Outline each Plasmodium ovale-infected red blood cell.
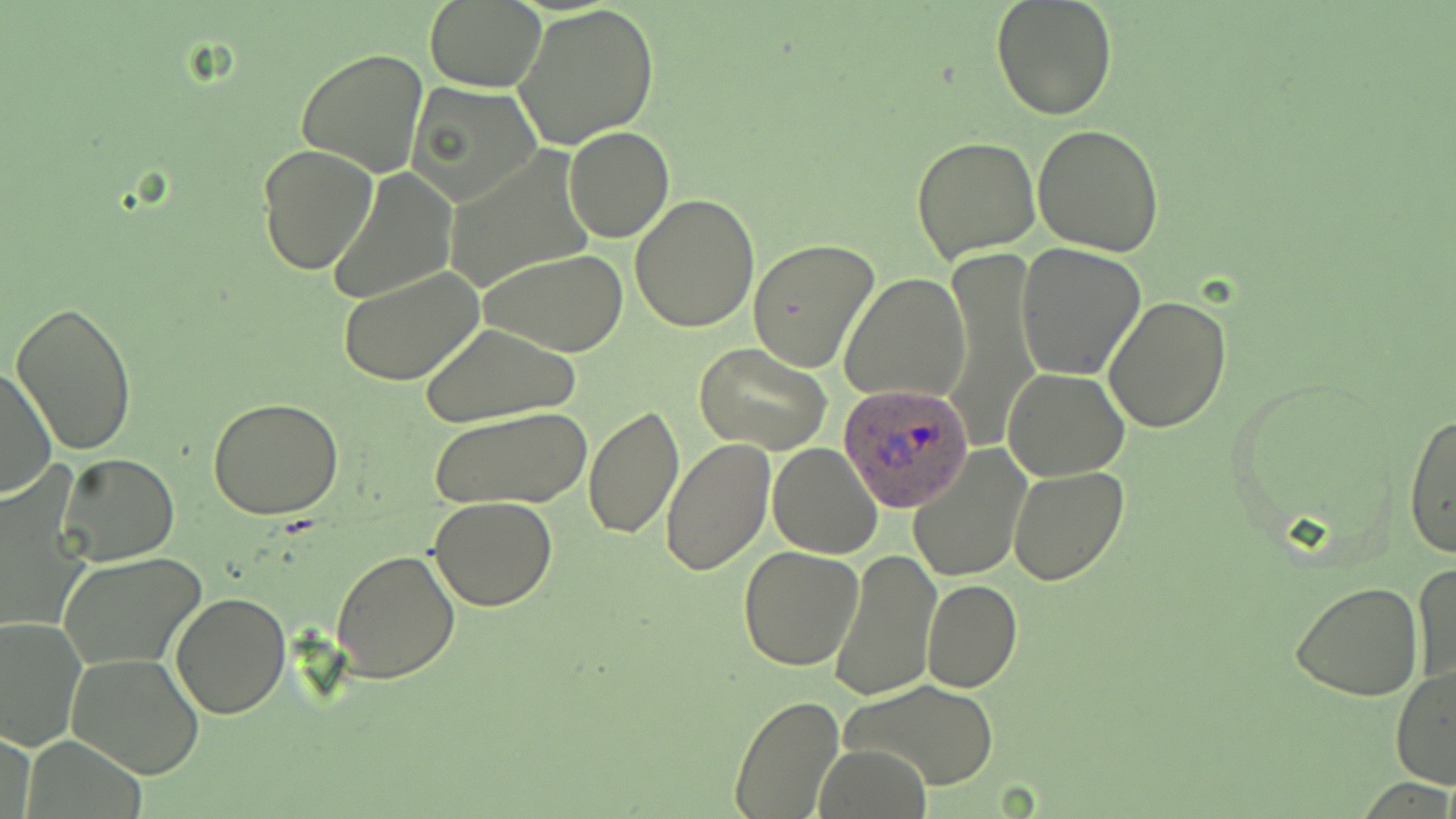
Approximate bounding boxes as (x1,y1)-(x2,y2) corner pairs in pixels.
Plasmodium ovale-infected red blood cells: (837,381)-(974,512).

Summary:
  - Uninfected red blood cell locations: (425,0)-(545,92), (989,0)-(1118,121), (513,2)-(662,148), (295,47)-(428,176), (406,81)-(543,208), (1032,121)-(1166,257), (563,127)-(674,243), (911,135)-(1042,264), (257,145)-(379,278), (444,150)-(598,294), (325,169)-(457,304), (629,193)-(760,332), (748,238)-(880,371), (1016,243)-(1147,380), (945,245)-(1039,448), (481,249)-(628,357), (335,265)-(487,386), (839,273)-(969,404), (1103,295)-(1233,433), (10,301)-(140,456), (421,323)-(580,427), (695,343)-(833,454), (0,364)-(56,500), (1003,366)-(1130,480), (209,397)-(345,519), (585,405)-(684,541), (428,406)-(592,509), (1402,410)-(1456,559), (659,437)-(775,575), (767,441)-(883,558), (907,446)-(1031,583), (57,453)-(178,565), (1008,465)-(1128,585), (1,474)-(92,635), (428,497)-(558,611), (738,545)-(865,670), (829,548)-(942,697), (330,549)-(461,684), (56,552)-(206,670), (1411,560)-(1455,691), (921,578)-(1023,693), (1290,579)-(1424,700), (170,592)-(291,720), (0,615)-(90,752), (67,652)-(205,779), (1391,664)-(1456,792), (843,681)-(1000,792), (728,695)-(845,818), (2,728)-(37,819), (815,745)-(931,819)
  - Slide-level diagnosis: Plasmodium ovale
  - Image size: 1456×819 pixels
  - Magnification: 1000x
  - Field of view: single
  - Stain: May-Grünwald-Giemsa
  - Preparation: thin blood film
  - Modality: light microscopy